Assess the morphology of the red blood cells.
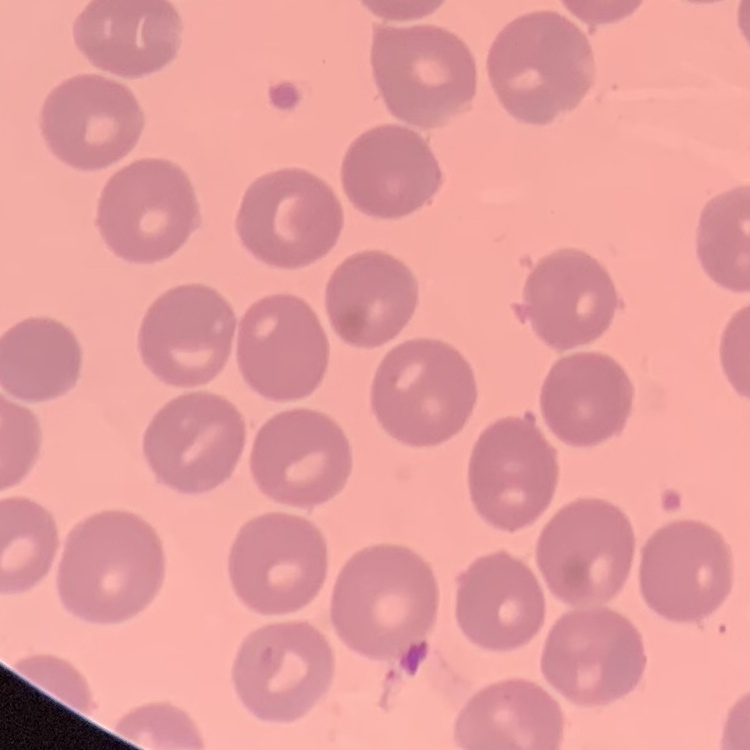
They show no rouleaux formation.

image_type: square crop of a larger photomicrograph
preparation: thin blood film
stain: Field's or Giemsa